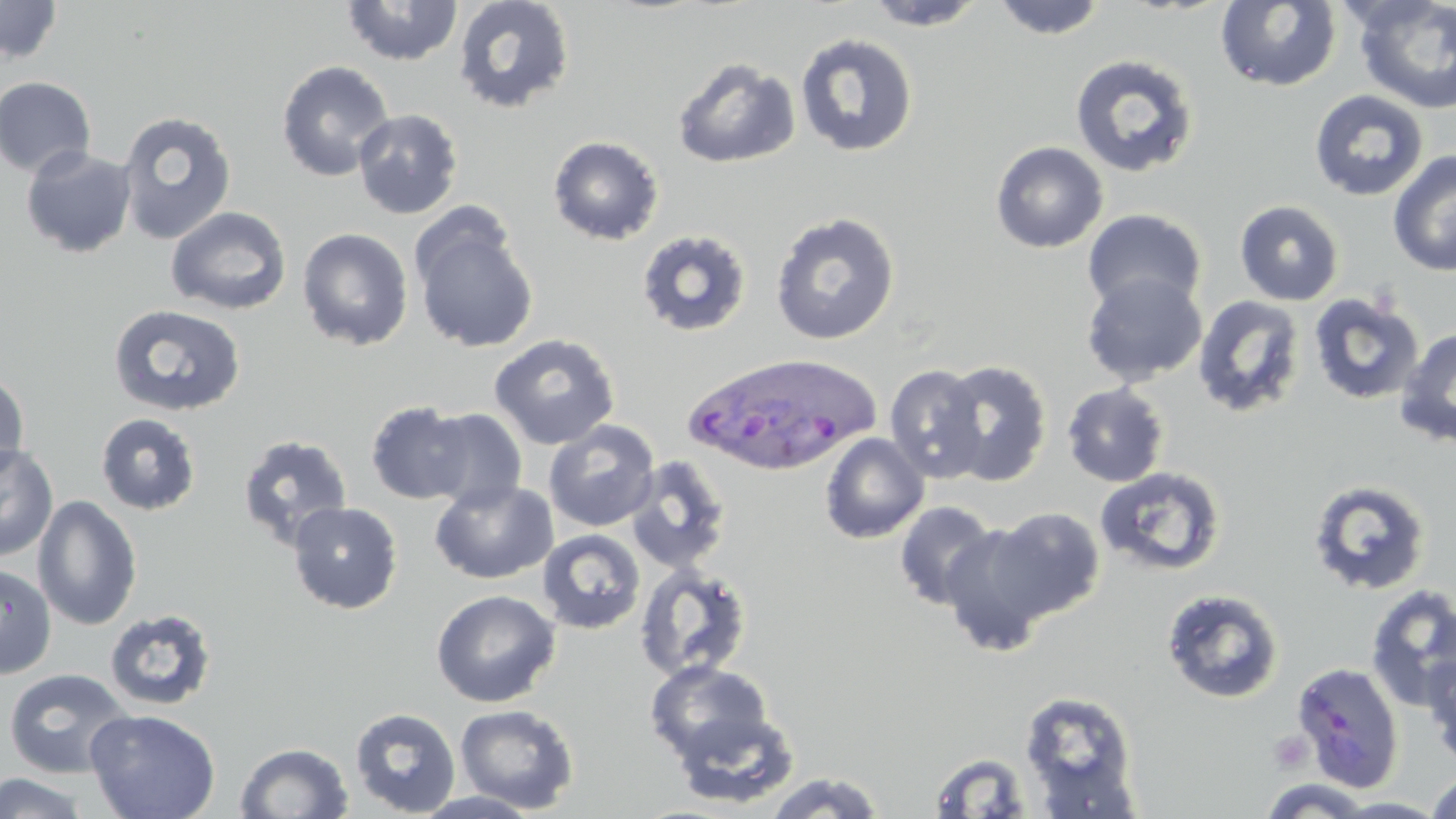
Approximate bounding boxes as (x1,y1)-(x2,y2) corner pairs in pixels. Uninfected red blood cell locations: (341,0)-(464,66), (991,0)-(1109,40), (0,1)-(63,65), (452,1)-(575,115), (859,1)-(992,31), (1216,1)-(1342,92), (1351,1)-(1456,115), (795,33)-(919,158), (1070,54)-(1201,178), (671,58)-(801,169), (275,60)-(395,181), (0,76)-(97,179), (1309,90)-(1429,202), (352,108)-(464,219), (116,110)-(237,245), (548,135)-(665,245), (990,141)-(1108,253), (20,146)-(137,258), (1387,150)-(1456,276), (1235,200)-(1344,306), (165,206)-(292,315), (1082,209)-(1207,314), (770,211)-(901,345), (411,213)-(539,354), (297,227)-(414,351), (635,229)-(752,338), (1081,272)-(1207,387), (1308,292)-(1425,405), (1192,295)-(1306,419), (108,303)-(246,416), (1395,326)-(1456,448), (489,333)-(620,450), (936,359)-(1052,486), (885,364)-(989,483), (0,370)-(30,484), (1061,383)-(1170,487), (366,400)-(474,505), (419,408)-(528,511), (95,413)-(201,515), (543,419)-(661,532), (237,433)-(354,551), (819,433)-(929,544), (0,444)-(59,562), (624,455)-(733,574), (1094,466)-(1227,577), (1307,478)-(1433,597), (429,479)-(557,584), (33,494)-(142,631), (286,500)-(403,614), (893,500)-(1000,610), (984,507)-(1106,622), (938,522)-(1058,654), (537,529)-(647,635), (0,562)-(57,679), (633,563)-(754,684), (1364,584)-(1456,712), (1161,588)-(1285,704), (430,589)-(560,707), (103,608)-(218,712), (1422,650)-(1456,773), (643,660)-(775,765), (1291,661)-(1405,792), (3,668)-(134,779), (1019,689)-(1142,813), (455,704)-(579,813), (350,707)-(461,817), (85,708)-(221,819), (670,708)-(801,809), (234,742)-(354,819), (926,751)-(1039,818), (1424,770)-(1456,819), (762,771)-(887,818), (0,772)-(92,819), (1257,779)-(1377,817), (412,790)-(546,818), (1328,796)-(1451,818). Platelet locations: (1268,731)-(1314,773). Plasmodium ovale-infected red blood cell locations: (682,352)-(882,479). Slide-level diagnosis: Plasmodium ovale. Single field of view. Light microscopy. May-Grünwald-Giemsa stain. Thin blood smear. 1000x magnification. Image is 1456×819 pixels.